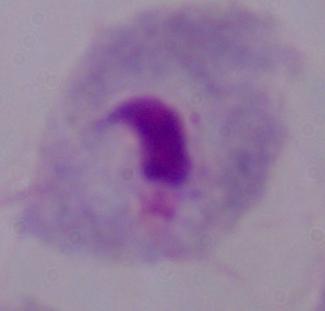
Micrograph. A trichomonad is seen. 1000x magnification.